Assess this cell for malaria.
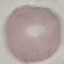
It is uninfected.

Summary:
  - Stain: Giemsa
  - Image type: cell patch, automatically extracted from a larger field of view and resized to 64 × 64 pixels
  - Capture: smartphone through the microscope eyepiece
  - Preparation: thin blood smear